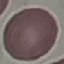

Summary:
  - Malaria status: uninfected
  - Preparation: thin blood film
  - Stain: Giemsa
  - Capture: smartphone through the microscope eyepiece
  - Image type: automatically extracted cell patch, resized to 64 × 64 pixels